State which parasite is depicted.
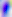
Toxoplasma gondii.

Photomicrograph. 400x magnification.